Locate the red blood cells and classify each one as Plasmodium falciparum-infected, uninfected, or of indeterminate infection status.
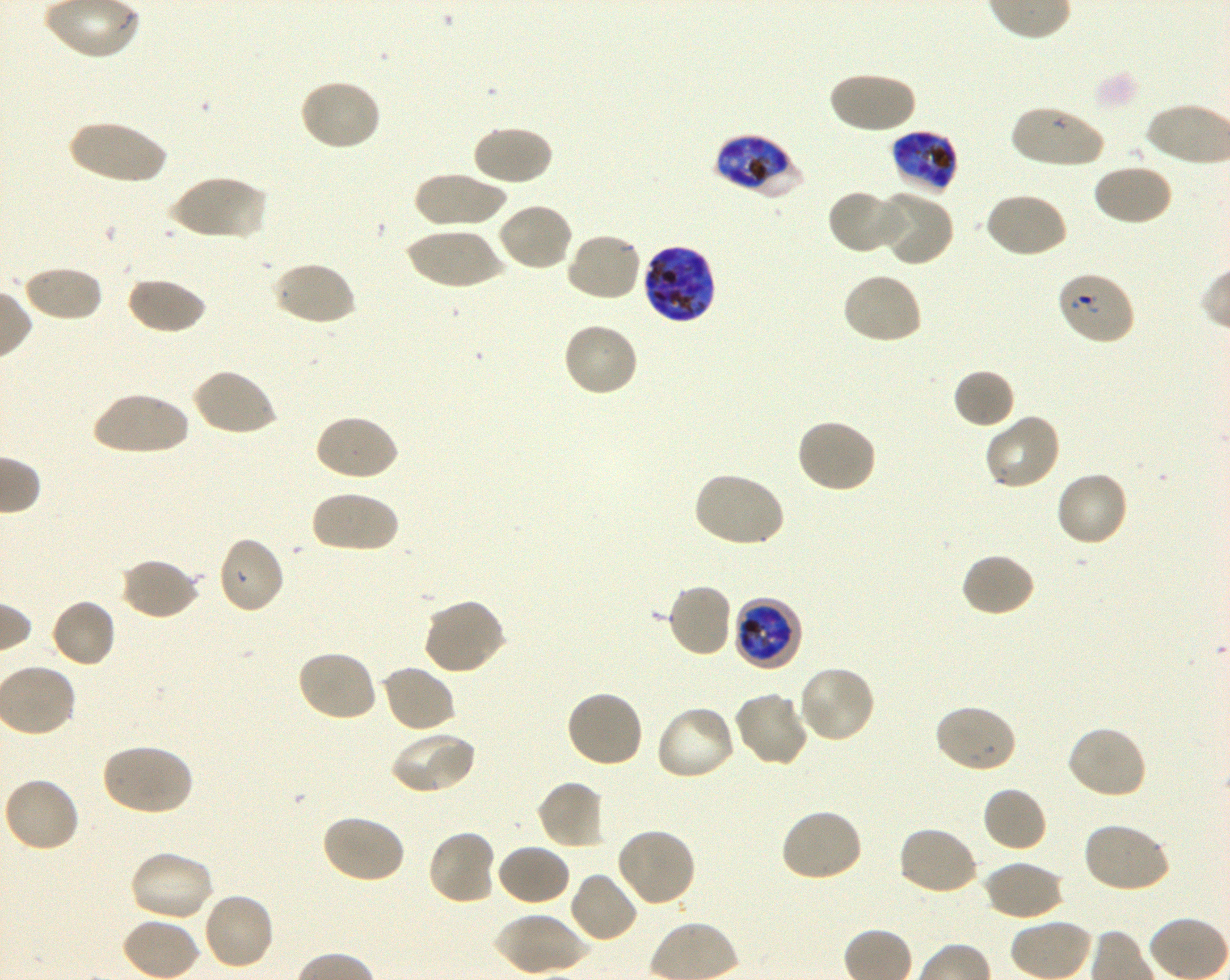
Approximate bounding rectangles given as corner coordinates in pixels from the top-left. Not every red blood cell is marked. A life-cycle stage — or a range of stages, where the recorded stages span more than one — follows each staged infected red blood cell.
Infected red blood cells: (x1=892, y1=130, x2=957, y2=194) late trophozoite to late schizont; (x1=714, y1=134, x2=803, y2=200) late trophozoite to late schizont; (x1=642, y1=243, x2=717, y2=325) late trophozoite to late schizont; (x1=733, y1=596, x2=804, y2=671) early trophozoite to early schizont.
Red blood cells of indeterminate infection status: (x1=1055, y1=270, x2=1136, y2=346).
Uninfected red blood cells: (x1=828, y1=70, x2=916, y2=135), (x1=298, y1=77, x2=382, y2=152), (x1=1009, y1=105, x2=1107, y2=169), (x1=67, y1=120, x2=169, y2=186), (x1=472, y1=124, x2=554, y2=187), (x1=1091, y1=163, x2=1173, y2=227), (x1=412, y1=171, x2=507, y2=228), (x1=168, y1=173, x2=265, y2=241), (x1=827, y1=189, x2=904, y2=254), (x1=875, y1=190, x2=954, y2=266), (x1=982, y1=191, x2=1067, y2=259), (x1=496, y1=202, x2=574, y2=273), (x1=403, y1=228, x2=507, y2=289), (x1=564, y1=230, x2=643, y2=303), (x1=271, y1=260, x2=357, y2=327), (x1=22, y1=264, x2=103, y2=322), (x1=841, y1=272, x2=924, y2=346), (x1=126, y1=275, x2=206, y2=335), (x1=562, y1=321, x2=640, y2=397), (x1=191, y1=367, x2=278, y2=437), (x1=953, y1=368, x2=1015, y2=429), (x1=91, y1=390, x2=190, y2=457), (x1=313, y1=413, x2=399, y2=482), (x1=983, y1=413, x2=1062, y2=492), (x1=795, y1=418, x2=878, y2=494), (x1=1054, y1=470, x2=1130, y2=548), (x1=693, y1=471, x2=786, y2=549), (x1=310, y1=489, x2=399, y2=554), (x1=215, y1=535, x2=286, y2=615), (x1=959, y1=552, x2=1036, y2=618), (x1=119, y1=558, x2=200, y2=621), (x1=666, y1=582, x2=734, y2=658), (x1=422, y1=596, x2=508, y2=676), (x1=50, y1=597, x2=118, y2=668), (x1=295, y1=649, x2=379, y2=722), (x1=379, y1=663, x2=457, y2=734), (x1=796, y1=665, x2=877, y2=745), (x1=564, y1=689, x2=644, y2=769), (x1=733, y1=690, x2=809, y2=769), (x1=933, y1=703, x2=1017, y2=775), (x1=655, y1=704, x2=738, y2=781), (x1=1066, y1=725, x2=1148, y2=801), (x1=388, y1=730, x2=477, y2=796), (x1=101, y1=742, x2=194, y2=817), (x1=2, y1=777, x2=81, y2=854), (x1=535, y1=779, x2=606, y2=850), (x1=981, y1=786, x2=1046, y2=853), (x1=779, y1=807, x2=864, y2=884), (x1=320, y1=813, x2=406, y2=884), (x1=1082, y1=821, x2=1172, y2=894), (x1=896, y1=825, x2=979, y2=897), (x1=615, y1=826, x2=697, y2=907), (x1=426, y1=829, x2=498, y2=906), (x1=495, y1=843, x2=572, y2=906), (x1=128, y1=849, x2=213, y2=923), (x1=983, y1=859, x2=1066, y2=921), (x1=568, y1=870, x2=639, y2=944), (x1=201, y1=891, x2=276, y2=972), (x1=493, y1=912, x2=592, y2=975).

Summary:
  - Stain: Giemsa
  - Culture: in-vitro Plasmodium falciparum strain 3D7, shaking
  - Objective: 100x, oil immersion, numerical aperture 1.30
  - Donor blood group: O+
  - Image size: 1230×980 pixels
  - Field of view: one from this slide
  - Preparation: thin blood film